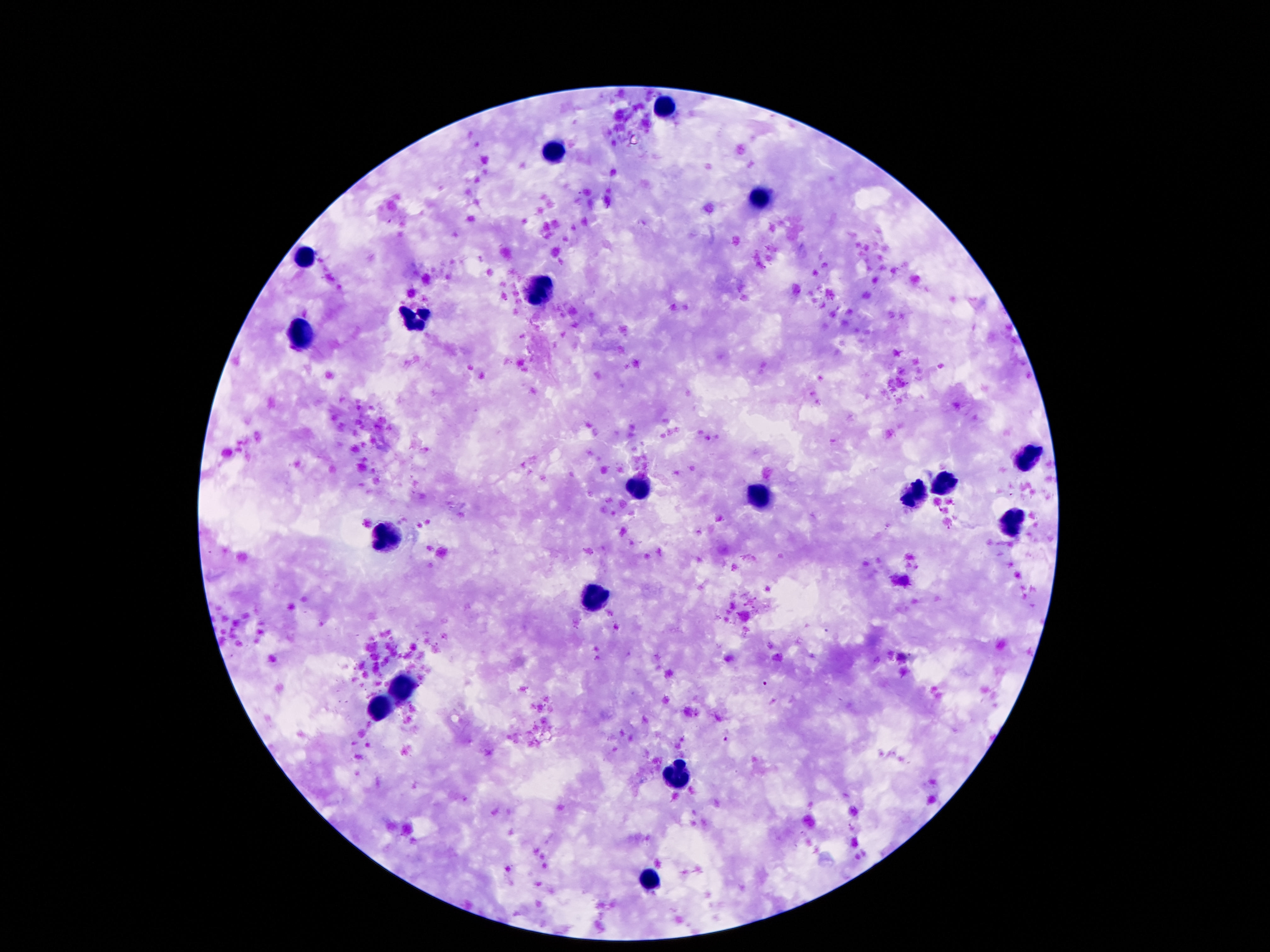

Approximate centers as [x, y] in pixels.
Summary:
  - Leukocyte locations: [663, 105], [552, 150], [755, 199], [302, 256], [540, 286], [417, 316], [300, 335], [1030, 458], [944, 481], [636, 491], [757, 495], [913, 495], [1011, 523], [382, 536], [593, 594], [399, 687], [382, 709], [681, 776], [653, 881]
  - Capture: smartphone camera through the microscope eyepiece
  - Image size: 1270×952 pixels
  - Magnification: 100x
  - Field of view: one from this slide
  - Preparation: thick peripheral-blood smear
  - Patient malaria status: uninfected
  - Stain: Giemsa